Mark where platelets are.
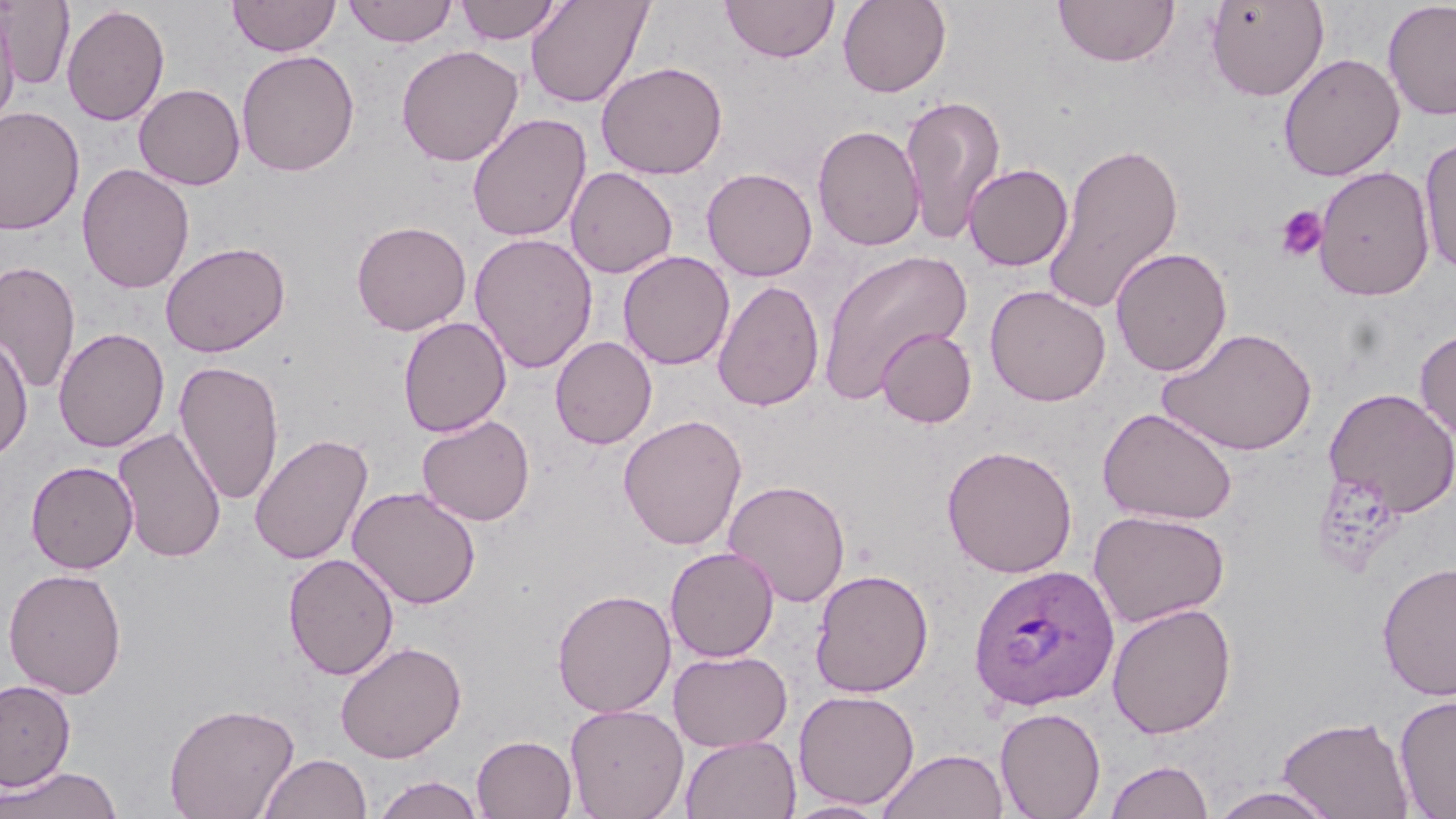
Approximate bounding boxes as (x1, y1, x2, y2) in pixels.
Platelets: (1274, 205, 1329, 262).

slide_level_diagnosis: Plasmodium ovale
stain: May-Grünwald-Giemsa
field_of_view: single
plasmodium_ovale_infected_red_blood_cell_locations: 'approximate bounding boxes as (x1, y1, x2, y2) in pixels: (968, 563, 1119, 711)'
magnification: 1000x
preparation: thin blood film
uninfected_red_blood_cell_locations: 'approximate bounding boxes as (x1, y1, x2, y2) in pixels: (1, 0, 75, 89), (228, 0, 340, 57), (342, 0, 458, 47), (455, 0, 563, 45), (721, 0, 839, 63), (837, 0, 951, 98), (1206, 0, 1329, 101), (524, 1, 653, 109), (1052, 1, 1179, 68), (1383, 2, 1456, 120), (61, 4, 170, 126), (0, 8, 20, 129), (396, 45, 523, 167), (236, 49, 360, 177), (1278, 53, 1404, 181), (596, 61, 728, 179), (134, 83, 245, 190), (899, 93, 1007, 245), (0, 106, 84, 235), (467, 113, 591, 242), (812, 124, 925, 251), (1419, 137, 1456, 275), (1043, 139, 1184, 316), (77, 163, 195, 293), (963, 163, 1073, 271), (1314, 165, 1435, 301), (565, 166, 678, 279), (701, 167, 817, 281), (351, 220, 472, 335), (469, 232, 598, 374), (160, 241, 290, 358), (1110, 247, 1232, 377), (817, 249, 973, 404), (618, 250, 735, 370), (1, 261, 81, 395), (712, 279, 825, 412), (984, 285, 1111, 406), (397, 316, 511, 436), (1158, 326, 1318, 456), (53, 327, 170, 453), (876, 327, 976, 428), (1415, 327, 1456, 442), (0, 333, 34, 461), (550, 336, 657, 449), (174, 361, 284, 505), (1323, 387, 1456, 517), (1098, 406, 1238, 525), (416, 414, 536, 526), (618, 414, 748, 550), (112, 426, 226, 562), (249, 433, 373, 566), (941, 444, 1078, 578), (25, 460, 138, 574), (722, 479, 851, 608), (347, 486, 482, 609), (1089, 509, 1230, 627), (665, 546, 779, 662), (283, 552, 399, 680), (1376, 561, 1456, 702), (3, 567, 127, 698), (810, 568, 933, 697), (552, 588, 677, 717), (1107, 602, 1237, 738), (335, 641, 467, 763), (669, 650, 792, 752), (0, 678, 76, 791), (793, 689, 920, 810), (1394, 694, 1456, 817), (163, 701, 300, 819), (565, 703, 689, 819), (995, 706, 1106, 819), (1276, 714, 1415, 819), (680, 734, 800, 818), (472, 735, 577, 818), (878, 748, 1008, 819), (258, 752, 371, 819), (1104, 758, 1215, 819), (0, 766, 123, 819), (372, 775, 486, 818), (1206, 785, 1341, 819), (782, 799, 892, 818)'
image_size: 1456×819 pixels
modality: optical microscopy